Locate every blood parasite and identify its species.
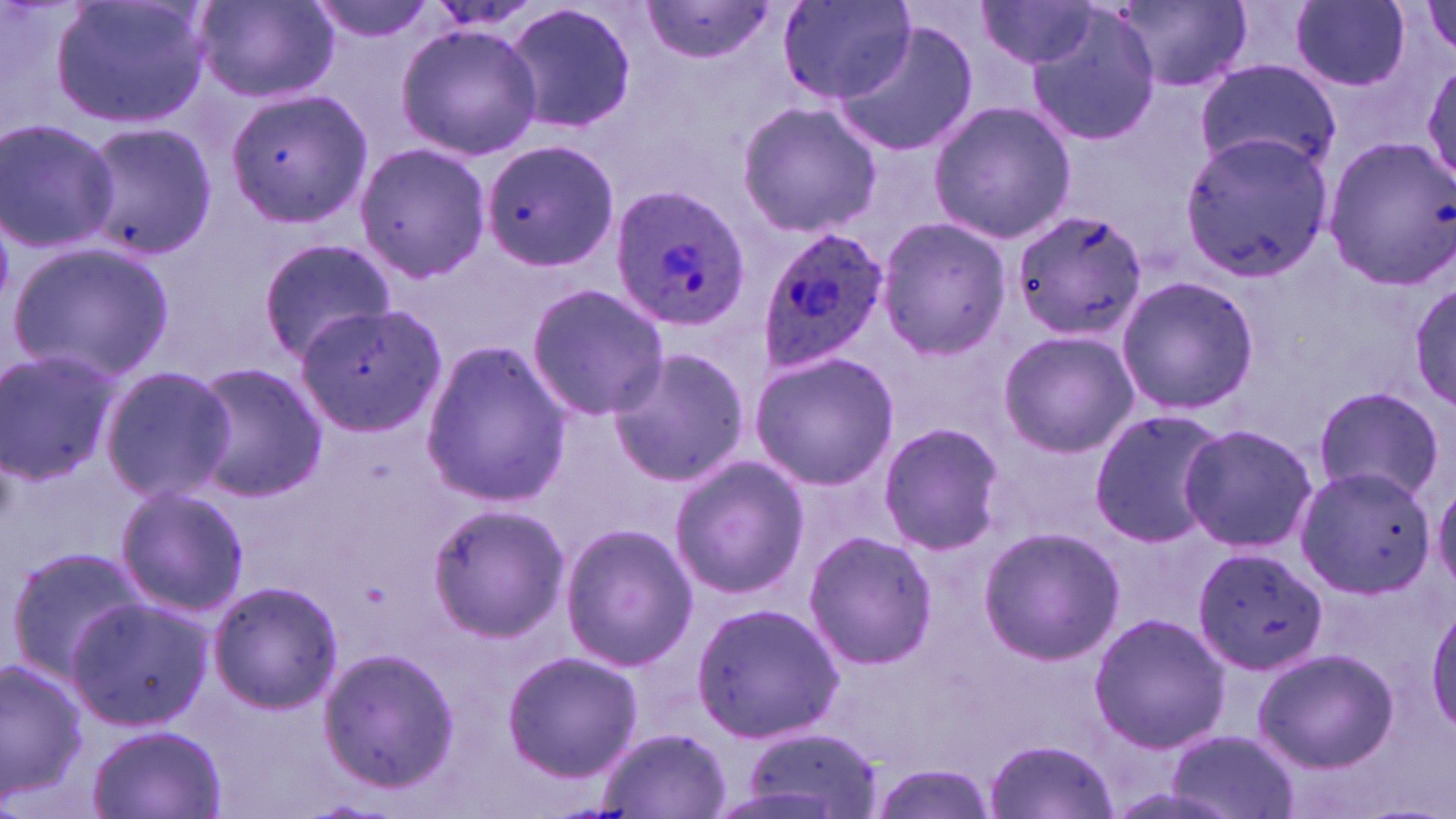

Approximate bounding boxes as (x1, y1, x2, y2) in pixels.
Plasmodium ovale-infected red blood cells: (609, 184, 751, 329), (755, 224, 889, 374).
No Plasmodium falciparum, Plasmodium malariae, Plasmodium vivax, Babesia divergens, or Trypanosoma brucei observed.

Uninfected red blood cell locations: (50, 0, 213, 128), (190, 0, 343, 104), (307, 0, 439, 43), (504, 1, 638, 137), (777, 1, 916, 104), (1284, 1, 1416, 94), (637, 3, 779, 64), (975, 3, 1100, 70), (1116, 3, 1249, 91), (1415, 3, 1456, 59), (1024, 10, 1165, 148), (394, 23, 542, 161), (832, 23, 976, 155), (1422, 59, 1455, 192), (1193, 60, 1340, 174), (230, 86, 376, 238), (736, 100, 883, 237), (927, 100, 1074, 243), (0, 120, 120, 253), (77, 123, 218, 261), (1180, 133, 1332, 274), (1323, 135, 1455, 286), (480, 139, 620, 272), (353, 141, 491, 284), (1012, 209, 1148, 343), (875, 216, 1011, 359), (257, 238, 394, 361), (8, 242, 172, 381), (1115, 274, 1257, 418), (1408, 276, 1456, 414), (526, 283, 669, 420), (272, 285, 440, 440), (996, 329, 1138, 458), (420, 343, 570, 507), (608, 347, 751, 489), (0, 349, 120, 486), (749, 350, 900, 490), (184, 362, 328, 501), (98, 366, 236, 503), (1313, 385, 1448, 504), (1088, 410, 1226, 546), (877, 421, 1004, 556), (1176, 422, 1318, 555), (669, 457, 808, 598), (1294, 466, 1436, 595), (1430, 476, 1456, 594), (113, 484, 249, 615), (426, 502, 572, 642), (559, 524, 698, 670), (977, 525, 1125, 666), (802, 529, 937, 671), (6, 546, 149, 680), (1192, 546, 1326, 675), (208, 580, 343, 712), (63, 597, 210, 732), (692, 601, 841, 746), (1428, 601, 1456, 733), (1089, 611, 1230, 754), (320, 646, 460, 791), (1252, 646, 1398, 772), (501, 649, 641, 780), (0, 656, 89, 802), (86, 724, 227, 819), (734, 727, 885, 817), (1167, 728, 1298, 819), (595, 729, 730, 817), (985, 737, 1119, 819). Slide-level diagnosis: Plasmodium ovale. Light microscopy. May-Grünwald-Giemsa stain. One field of a larger specimen. Thin blood smear. 1000x magnification. Image is 1456×819 pixels.